State which parasite is depicted.
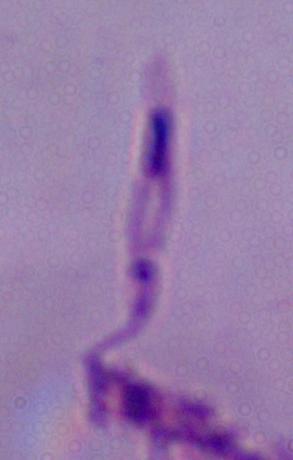

Leishmania.

Micrograph. 1000x magnification.